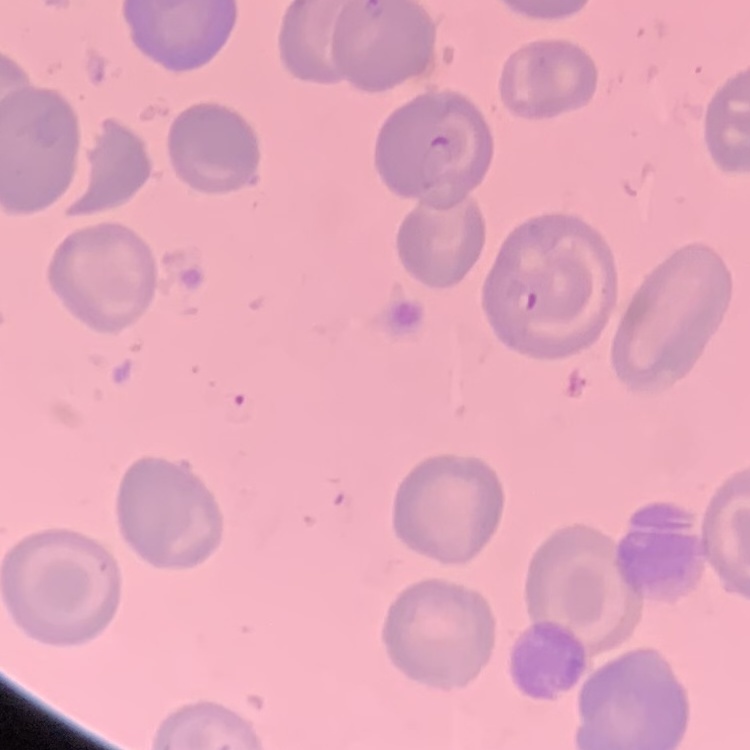
Summary:
  - Erythrocyte morphology: no rouleaux formation
  - Stain: Field's or Giemsa
  - Image type: square crop of a larger photomicrograph
  - Preparation: thin blood smear